Locate every malaria parasite.
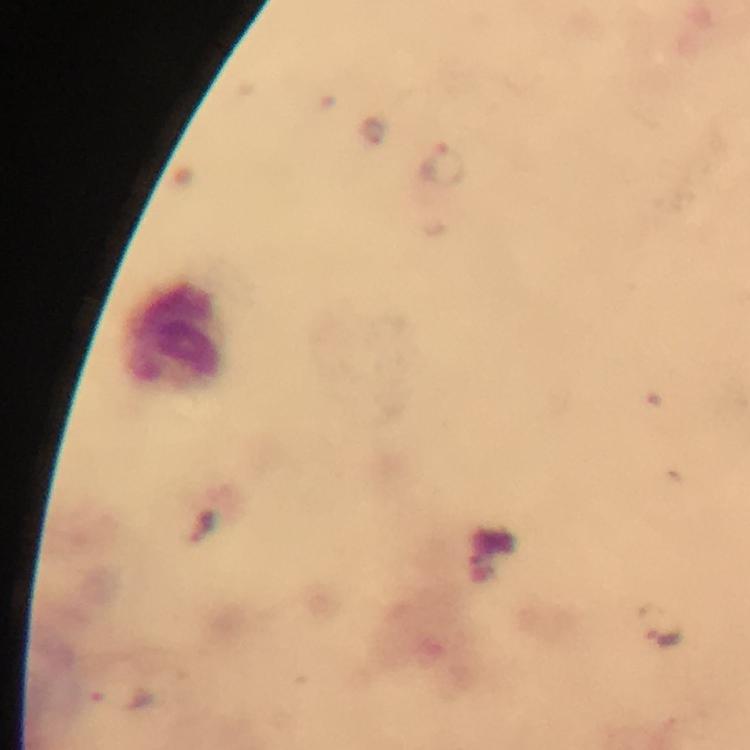
Approximate centers as {x, y} in pixels.
Malaria parasites: {376, 131}, {442, 165}, {665, 635}, {126, 698}.

Summary:
  - Leukocyte locations: {176, 332}
  - Image size: 750×750 pixels
  - Stain: Giemsa
  - Context: from a malaria diagnostic workup
  - Cropped from: one field of view
  - Preparation: thick blood film
  - Capture: smartphone camera through the microscope
  - Magnification: 100x
  - Immersion oil: used